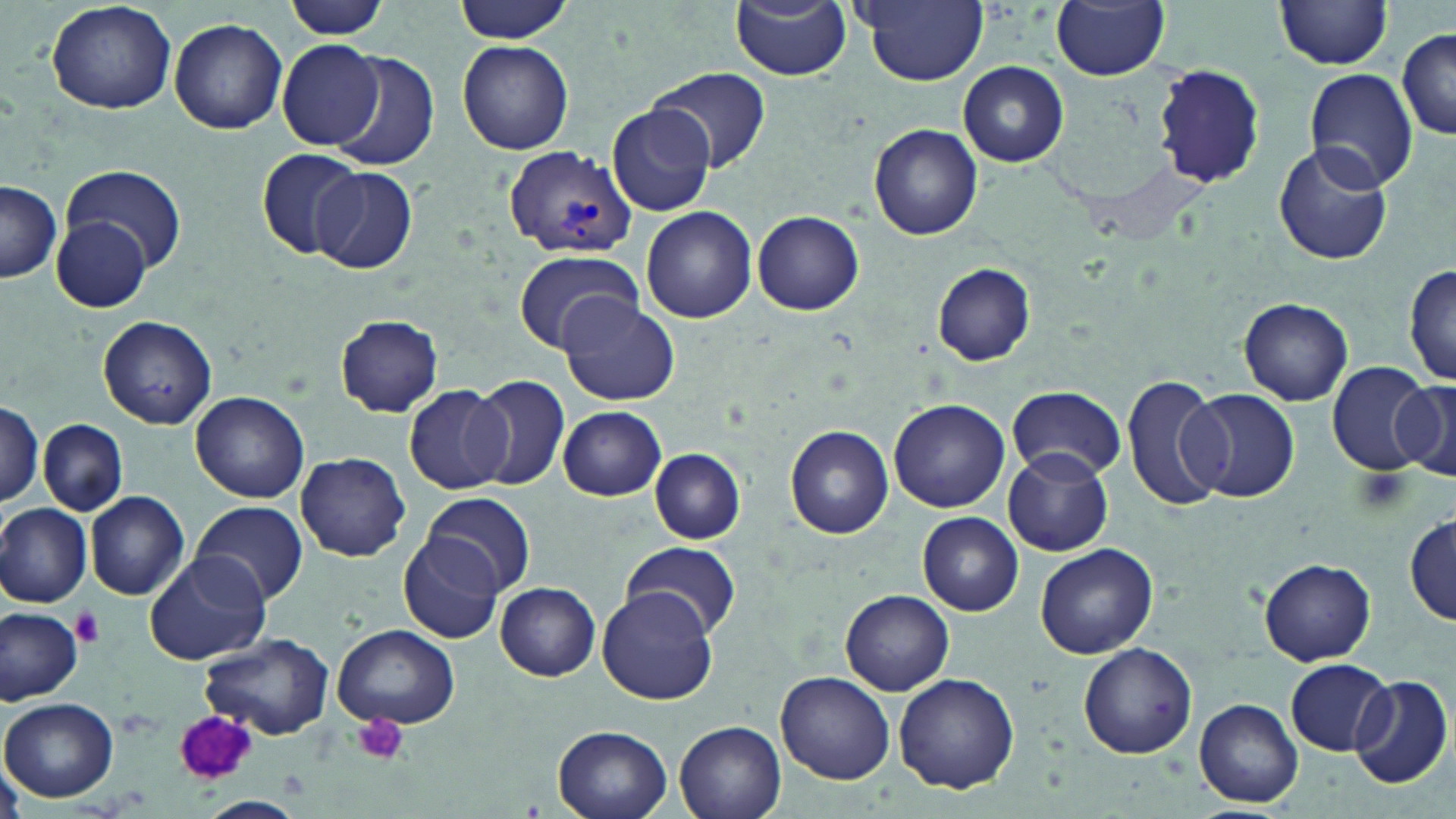

Approximate bounding boxes as named x1/y1/x2/y2 corners in pixels. Platelet locations: (x1=1354, y1=465, x2=1412, y2=516), (x1=71, y1=606, x2=105, y2=647), (x1=174, y1=712, x2=257, y2=782), (x1=354, y1=713, x2=409, y2=765). Uninfected red blood cell locations: (x1=45, y1=0, x2=177, y2=115), (x1=283, y1=0, x2=390, y2=42), (x1=453, y1=0, x2=577, y2=43), (x1=855, y1=0, x2=988, y2=87), (x1=1052, y1=0, x2=1170, y2=81), (x1=732, y1=1, x2=852, y2=81), (x1=1275, y1=1, x2=1395, y2=70), (x1=168, y1=18, x2=288, y2=134), (x1=1397, y1=30, x2=1456, y2=139), (x1=457, y1=39, x2=574, y2=155), (x1=279, y1=40, x2=386, y2=150), (x1=329, y1=51, x2=438, y2=171), (x1=959, y1=61, x2=1069, y2=166), (x1=1151, y1=64, x2=1265, y2=187), (x1=649, y1=69, x2=770, y2=173), (x1=1302, y1=69, x2=1419, y2=191), (x1=605, y1=103, x2=717, y2=218), (x1=868, y1=124, x2=982, y2=241), (x1=1273, y1=141, x2=1394, y2=267), (x1=257, y1=148, x2=366, y2=263), (x1=61, y1=163, x2=186, y2=274), (x1=312, y1=167, x2=417, y2=273), (x1=0, y1=182, x2=61, y2=285), (x1=642, y1=206, x2=756, y2=324), (x1=751, y1=210, x2=864, y2=315), (x1=48, y1=217, x2=156, y2=312), (x1=513, y1=248, x2=642, y2=353), (x1=933, y1=262, x2=1034, y2=366), (x1=1403, y1=263, x2=1456, y2=390), (x1=559, y1=295, x2=679, y2=406), (x1=1238, y1=297, x2=1354, y2=406), (x1=98, y1=315, x2=216, y2=428), (x1=335, y1=315, x2=443, y2=417), (x1=1324, y1=361, x2=1438, y2=476), (x1=470, y1=373, x2=571, y2=491), (x1=1121, y1=373, x2=1230, y2=514), (x1=1391, y1=378, x2=1456, y2=481), (x1=404, y1=384, x2=513, y2=495), (x1=1006, y1=385, x2=1125, y2=481), (x1=1185, y1=390, x2=1300, y2=503), (x1=191, y1=391, x2=308, y2=502), (x1=888, y1=399, x2=1010, y2=513), (x1=0, y1=401, x2=44, y2=508), (x1=558, y1=406, x2=667, y2=500), (x1=39, y1=419, x2=128, y2=516), (x1=786, y1=424, x2=896, y2=539), (x1=650, y1=449, x2=744, y2=542), (x1=1002, y1=450, x2=1114, y2=557), (x1=296, y1=451, x2=411, y2=563), (x1=424, y1=490, x2=534, y2=596), (x1=84, y1=491, x2=189, y2=600), (x1=191, y1=500, x2=308, y2=606), (x1=0, y1=502, x2=92, y2=607), (x1=1404, y1=511, x2=1456, y2=624), (x1=918, y1=512, x2=1023, y2=616), (x1=398, y1=534, x2=503, y2=644), (x1=622, y1=541, x2=741, y2=639), (x1=1034, y1=543, x2=1159, y2=660), (x1=144, y1=549, x2=272, y2=665), (x1=1258, y1=558, x2=1376, y2=667), (x1=495, y1=582, x2=602, y2=680), (x1=597, y1=588, x2=720, y2=705), (x1=841, y1=589, x2=954, y2=694), (x1=0, y1=605, x2=84, y2=704), (x1=333, y1=623, x2=461, y2=729), (x1=201, y1=632, x2=334, y2=740), (x1=1077, y1=644, x2=1198, y2=759), (x1=1285, y1=659, x2=1394, y2=757), (x1=776, y1=671, x2=894, y2=785), (x1=892, y1=673, x2=1020, y2=793), (x1=1349, y1=676, x2=1452, y2=789), (x1=1194, y1=696, x2=1303, y2=807), (x1=2, y1=699, x2=118, y2=802), (x1=674, y1=722, x2=786, y2=819), (x1=552, y1=725, x2=673, y2=819), (x1=197, y1=796, x2=305, y2=818). Plasmodium vivax-infected red blood cell locations: (x1=504, y1=146, x2=638, y2=259). Slide-level diagnosis: Plasmodium vivax. Single field of view. Thin blood film. Optical microscopy. Image is 1456×819 pixels. May-Grünwald-Giemsa-stained preparation. Captured at 1000x magnification.